Locate and identify every blood parasite.
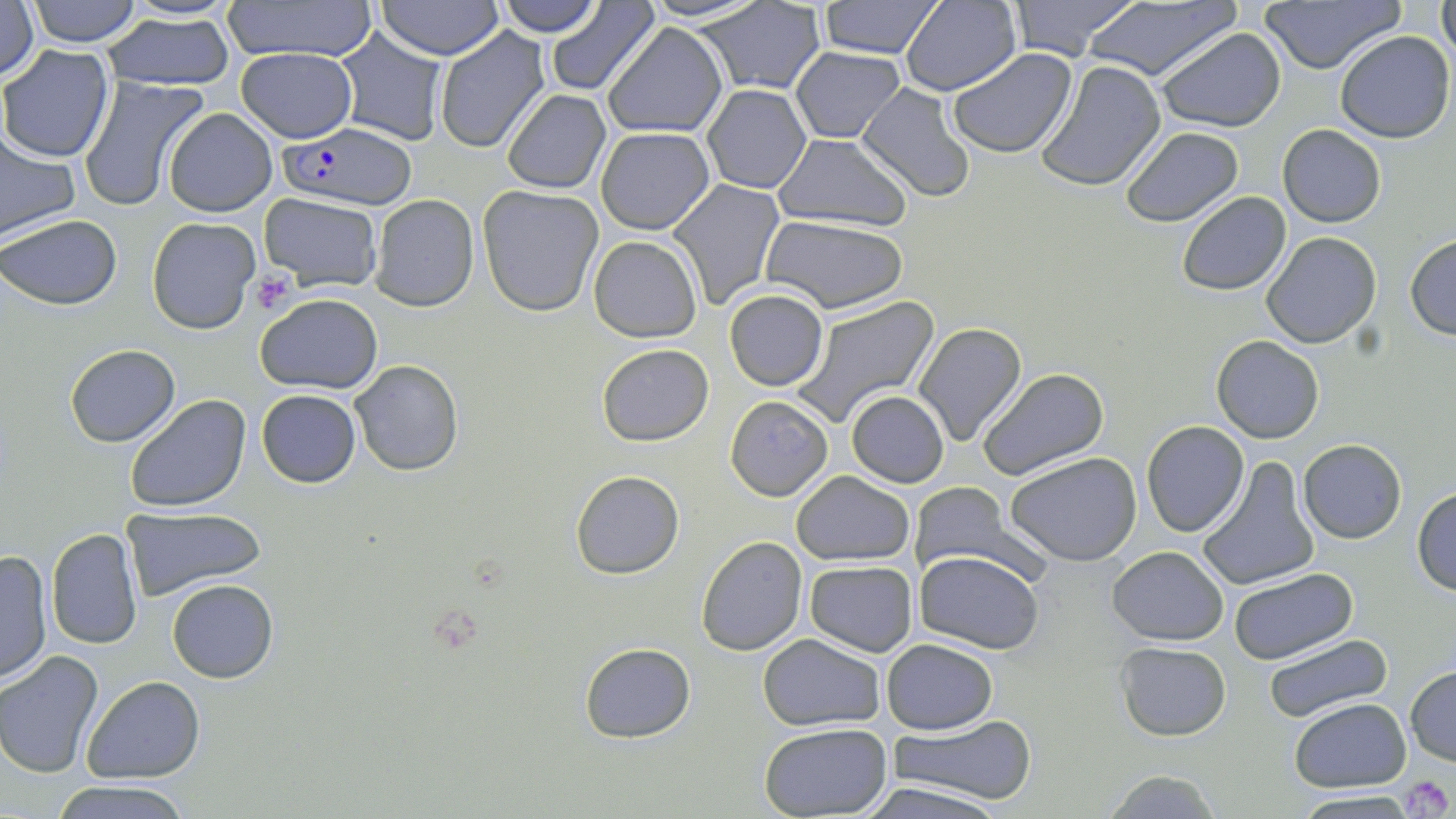
Approximate bounding boxes as (x1,y1)-(x2,y2) corner pairs in pixels.
Plasmodium falciparum-infected red blood cells: (281,123)-(416,210).
No Plasmodium ovale, Plasmodium malariae, Plasmodium vivax, Babesia divergens, or Trypanosoma brucei observed.

Uninfected red blood cell locations: (23,0)-(145,47), (108,0)-(243,22), (223,0)-(378,62), (494,0)-(605,38), (641,0)-(769,24), (818,0)-(946,60), (1005,0)-(1142,62), (1075,0)-(1240,82), (1260,0)-(1405,74), (1435,0)-(1456,60), (376,1)-(505,58), (691,1)-(827,95), (899,1)-(1020,96), (0,2)-(38,87), (544,2)-(660,93), (102,10)-(237,92), (601,22)-(730,137), (434,26)-(553,154), (335,28)-(448,145), (1154,28)-(1287,133), (1335,31)-(1454,143), (0,45)-(115,162), (790,46)-(906,142), (235,47)-(359,141), (947,47)-(1078,161), (878,58)-(1022,183), (1036,60)-(1166,193), (78,77)-(208,213), (702,84)-(813,195), (855,84)-(975,203), (502,90)-(611,194), (164,107)-(277,217), (1278,124)-(1385,227), (0,126)-(80,242), (596,126)-(715,235), (1119,126)-(1243,227), (773,133)-(911,231), (665,178)-(785,311), (477,185)-(604,318), (1176,192)-(1291,294), (257,193)-(384,292), (370,193)-(479,311), (758,213)-(910,314), (0,214)-(121,308), (147,217)-(261,333), (1262,231)-(1381,348), (1405,235)-(1456,339), (588,236)-(702,342), (725,289)-(828,391), (255,291)-(384,395), (792,296)-(939,430), (913,322)-(1027,448), (1211,335)-(1325,442), (596,343)-(714,446), (64,344)-(180,447), (350,359)-(464,476), (977,367)-(1109,483), (255,389)-(362,487), (846,391)-(947,488), (124,394)-(253,514), (725,396)-(833,500), (1141,420)-(1249,537), (1297,438)-(1406,544), (1007,453)-(1142,566), (1197,458)-(1318,591), (572,471)-(684,578), (790,471)-(915,566), (912,483)-(1022,582), (1411,487)-(1456,594), (122,507)-(265,602), (46,528)-(143,649), (696,536)-(808,657), (1106,545)-(1229,646), (0,549)-(52,685), (914,551)-(1045,655), (805,560)-(917,656), (1229,568)-(1356,664), (167,579)-(278,684), (759,633)-(886,732), (1263,634)-(1392,722), (882,639)-(999,734), (1115,641)-(1231,740), (579,643)-(696,743), (0,650)-(104,776), (1406,665)-(1456,766), (81,676)-(203,783), (1290,698)-(1412,793), (892,716)-(1034,808), (758,722)-(892,816), (1102,769)-(1221,818), (51,780)-(192,819), (854,782)-(1010,819), (1291,790)-(1419,818). Platelet locations: (251,273)-(296,313), (1399,773)-(1451,818). Slide-level diagnosis: Plasmodium falciparum. Thin blood smear. One field of a larger specimen. Light microscopy. Image is 1456×819 pixels. Captured at 1000x magnification. May-Grünwald-Giemsa-stained preparation.